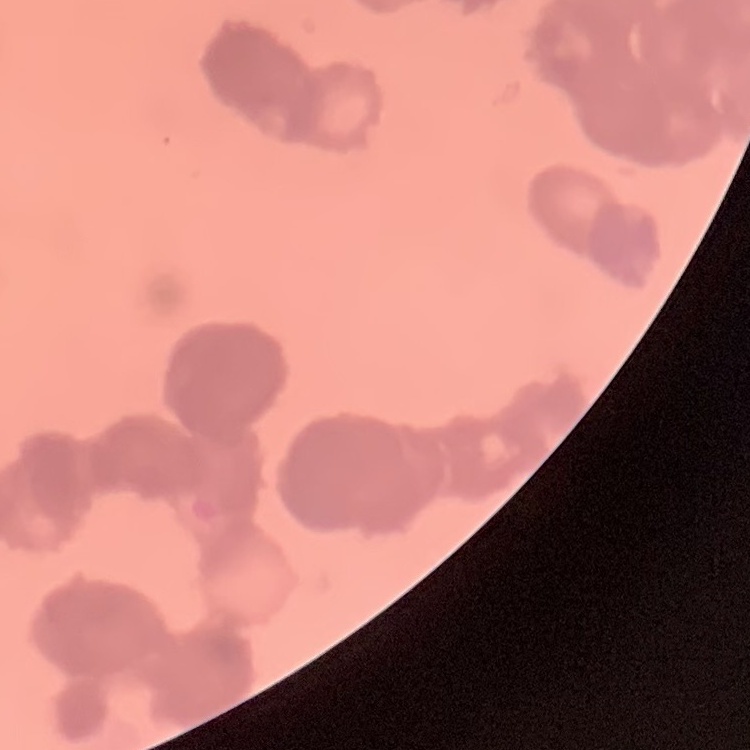

Summary:
  - Red blood cell morphology: rouleaux formation
  - Image type: square crop of a larger photomicrograph
  - Stain: Field's or Giemsa
  - Preparation: thin blood film